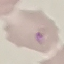

{
  "malaria_status": "parasitized",
  "stain": "Giemsa",
  "preparation": "thin blood smear",
  "image_type": "automatically extracted cell patch, resized to 64 × 64 pixels",
  "capture": "smartphone through the microscope eyepiece"
}